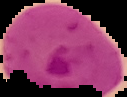

Image is 127×97 pixels. Malaria status: parasitized. The area outside the segmented cell region is set to black. From a thin blood smear.